Outline each uninfected red blood cell.
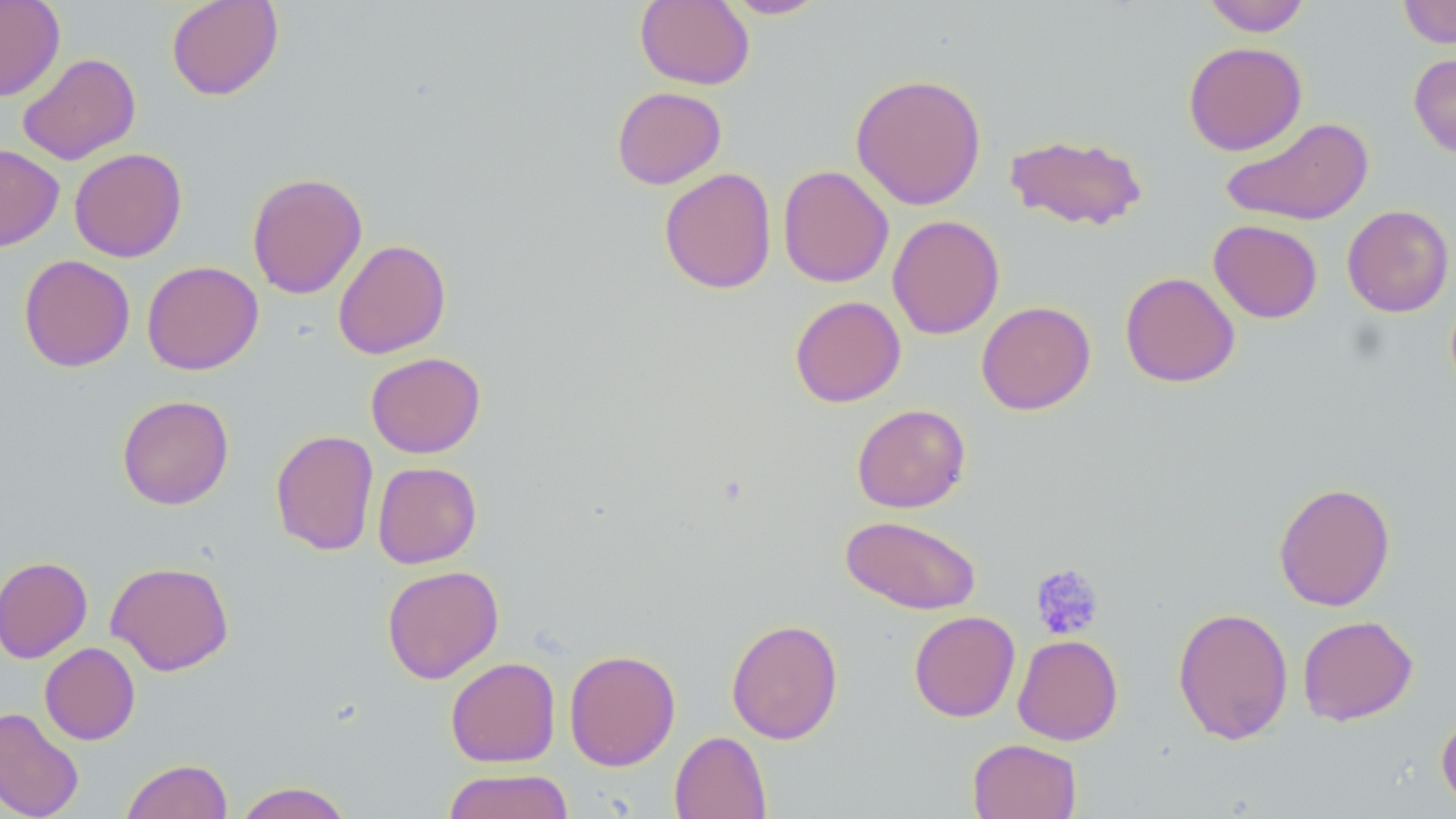
Approximate bounding boxes as named x1/y1/x2/y2 corners in pixels.
Uninfected red blood cells: (x1=0, y1=0, x2=65, y2=101), (x1=165, y1=0, x2=284, y2=101), (x1=635, y1=0, x2=755, y2=89), (x1=721, y1=0, x2=829, y2=19), (x1=1201, y1=0, x2=1311, y2=36), (x1=1398, y1=0, x2=1456, y2=48), (x1=1183, y1=41, x2=1307, y2=156), (x1=16, y1=52, x2=141, y2=165), (x1=1409, y1=52, x2=1456, y2=159), (x1=850, y1=72, x2=987, y2=210), (x1=611, y1=86, x2=727, y2=189), (x1=1221, y1=116, x2=1373, y2=226), (x1=1004, y1=133, x2=1148, y2=231), (x1=0, y1=144, x2=64, y2=252), (x1=69, y1=147, x2=187, y2=262), (x1=778, y1=165, x2=894, y2=288), (x1=659, y1=167, x2=777, y2=294), (x1=246, y1=172, x2=368, y2=299), (x1=1342, y1=205, x2=1455, y2=317), (x1=887, y1=214, x2=1004, y2=339), (x1=1208, y1=219, x2=1323, y2=323), (x1=333, y1=239, x2=451, y2=359), (x1=18, y1=254, x2=135, y2=372), (x1=142, y1=260, x2=264, y2=375), (x1=1120, y1=271, x2=1240, y2=387), (x1=789, y1=295, x2=906, y2=407), (x1=976, y1=301, x2=1095, y2=415), (x1=366, y1=351, x2=485, y2=458), (x1=117, y1=395, x2=234, y2=510), (x1=851, y1=403, x2=970, y2=513), (x1=270, y1=429, x2=379, y2=556), (x1=372, y1=461, x2=482, y2=568), (x1=1273, y1=481, x2=1396, y2=611), (x1=840, y1=515, x2=981, y2=615), (x1=0, y1=556, x2=92, y2=663), (x1=106, y1=560, x2=234, y2=676), (x1=381, y1=565, x2=504, y2=684), (x1=1172, y1=605, x2=1294, y2=746), (x1=908, y1=610, x2=1021, y2=722), (x1=1297, y1=614, x2=1418, y2=726), (x1=726, y1=618, x2=843, y2=744), (x1=1013, y1=634, x2=1123, y2=745), (x1=40, y1=642, x2=140, y2=745), (x1=564, y1=648, x2=680, y2=771), (x1=445, y1=657, x2=561, y2=767), (x1=0, y1=707, x2=84, y2=819), (x1=1436, y1=709, x2=1456, y2=811), (x1=669, y1=730, x2=772, y2=819), (x1=967, y1=738, x2=1082, y2=819), (x1=121, y1=759, x2=232, y2=819), (x1=442, y1=768, x2=575, y2=819), (x1=233, y1=781, x2=354, y2=819).

Summary:
  - Platelet locations: (x1=1030, y1=564, x2=1104, y2=640)
  - Slide-level diagnosis: no evidence of blood parasites
  - Stain: May-Grünwald-Giemsa
  - Modality: light microscopy
  - Image size: 1456×819 pixels
  - Magnification: 1000x
  - Field of view: single
  - Preparation: thin blood film